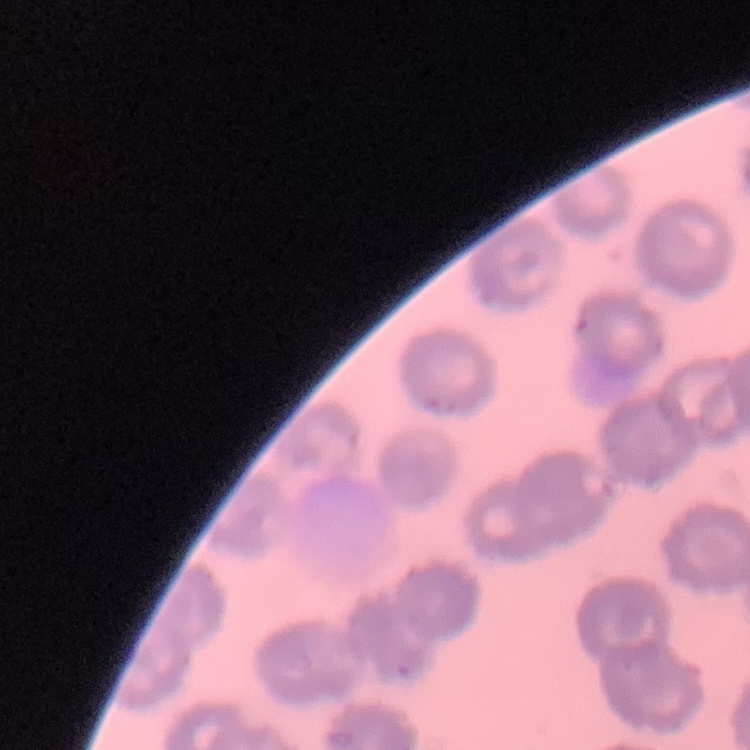

Summary:
  - Erythrocyte morphology: no rouleaux formation
  - Stain: Field's or Giemsa
  - Image type: one tile cut from a larger photomicrograph
  - Preparation: thin blood film